Identify the cell.
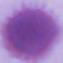
This is an erythrocyte.

{
  "modality": "photomicrograph",
  "magnification": "1000x"
}